Assess the morphology of the red blood cells.
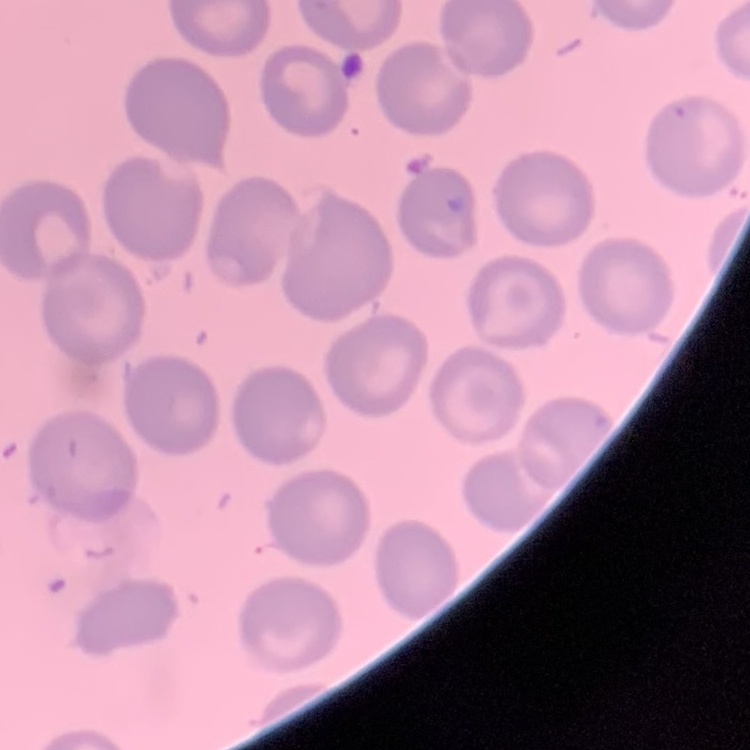

They show no rouleaux formation.

Square crop of a larger photomicrograph. Field's or Giemsa stain. Thin blood smear.